Give the position of every malaria parasite.
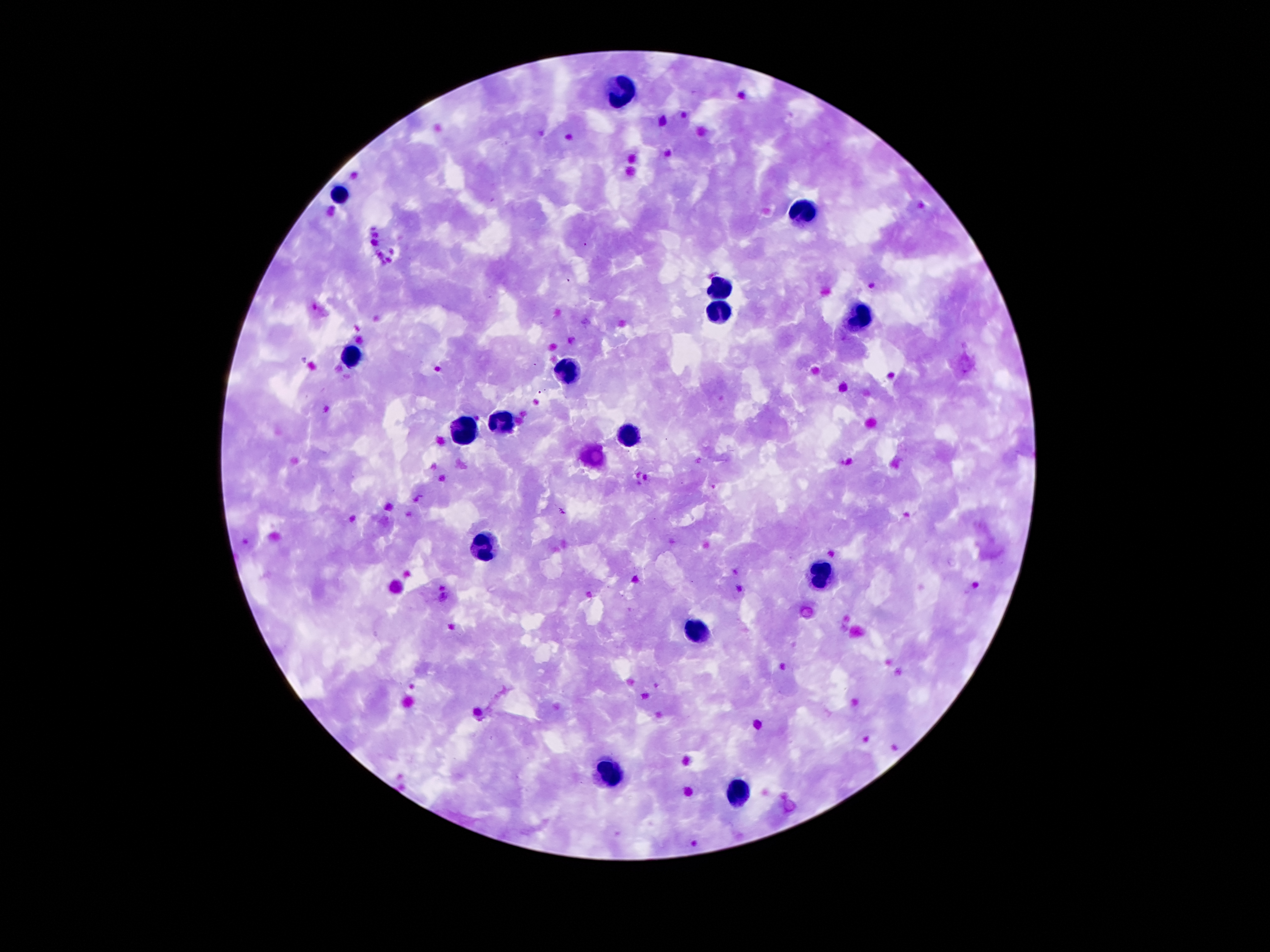

Approximate object centers, in pixels from the top-left corner.
Malaria parasites: (x=584, y=243), (x=872, y=283), (x=314, y=306), (x=561, y=511), (x=740, y=589), (x=443, y=595).

Leukocyte locations: (x=620, y=91), (x=341, y=192), (x=804, y=211), (x=718, y=288), (x=715, y=308), (x=858, y=320), (x=350, y=360), (x=567, y=372), (x=504, y=424), (x=466, y=433), (x=633, y=438), (x=481, y=547), (x=822, y=579), (x=697, y=633), (x=608, y=770), (x=735, y=792). Image is 1270×952 pixels. One field from this slide. Photographed through the microscope eyepiece with a smartphone camera. Giemsa-stained preparation. 100x magnification. Thick peripheral-blood smear. Patient malaria status: positive for Plasmodium falciparum.